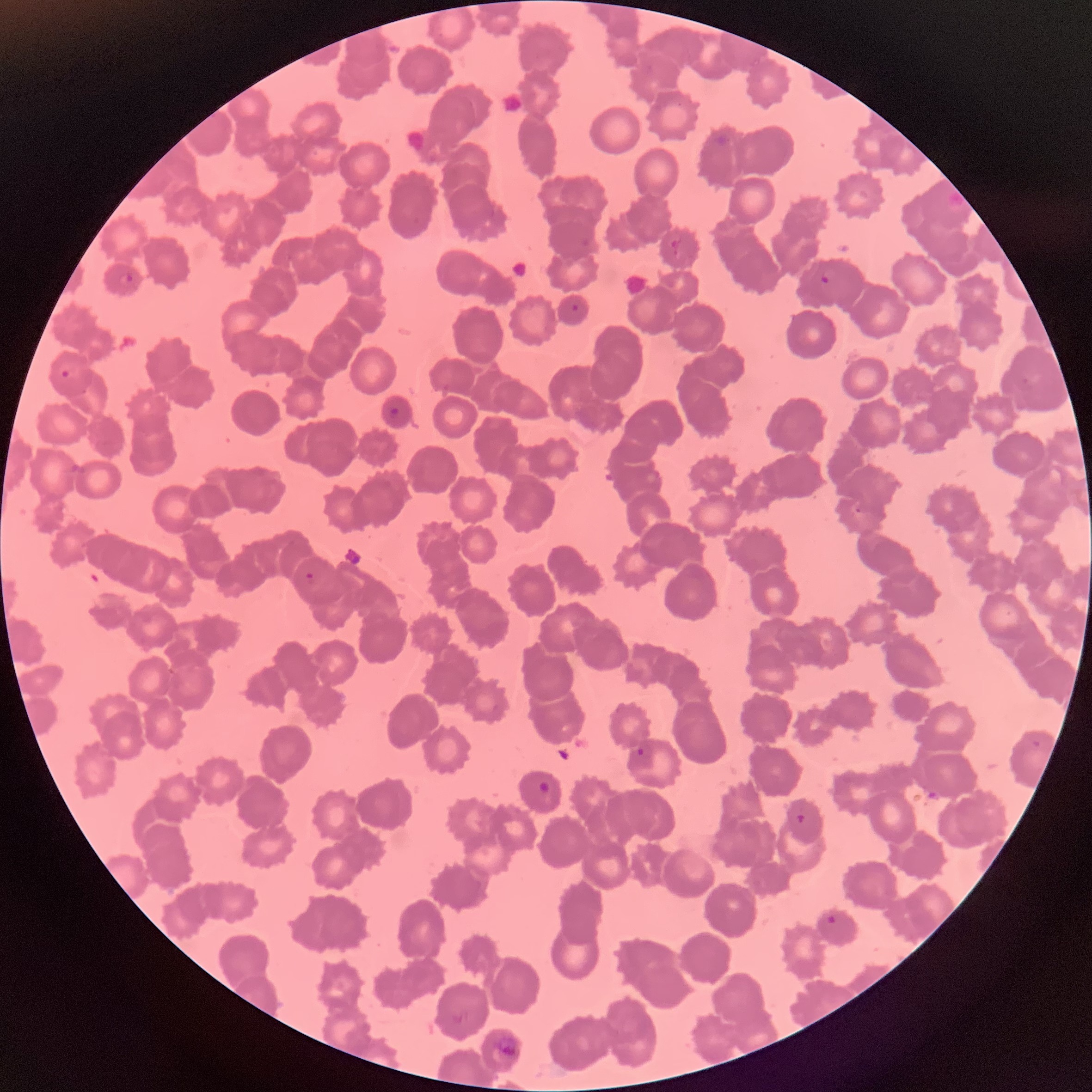

red_blood_cell_morphology: rouleaux formation
plasmodium_parasite_locations: 'approximate bounding boxes as [x1, y1, x2, y2] in pixels: [670, 238, 679, 249], [119, 273, 134, 285], [819, 274, 830, 284], [571, 303, 580, 312], [59, 362, 79, 380], [384, 405, 399, 419], [854, 504, 871, 515], [303, 571, 318, 582], [636, 746, 645, 757], [538, 781, 551, 795], [794, 813, 808, 826], [824, 913, 838, 928], [450, 1011, 467, 1026]'
preparation: thin blood film
image_size: 1092×1092 pixels
modality: optical microscopy